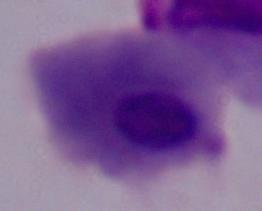
Photomicrograph. 1000x magnification. A trichomonad is shown.